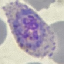
malaria status = parasitized
image type = automatically extracted cell patch, resized to 64 × 64 pixels
stain = Giemsa
preparation = thin blood film
capture = smartphone camera at the microscope eyepiece